Assess this cell for malaria.
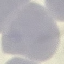
It is uninfected.

Summary:
  - Capture: smartphone camera at the microscope eyepiece
  - Stain: Giemsa
  - Image type: automatically extracted cell patch, resized to 64 × 64 pixels
  - Preparation: thin blood film